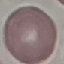

Malaria status: uninfected. Giemsa stain. Thin smear of blood. Automatically extracted cell patch, resized to 64 × 64 pixels. Acquired by smartphone through the microscope eyepiece.